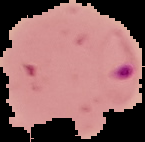 Malaria status: parasitized. From a thin blood smear. Image is 145×142 pixels. Cell region segmented out of the field of view; the surrounding area is masked to black.